Assess the morphology of the red blood cells.
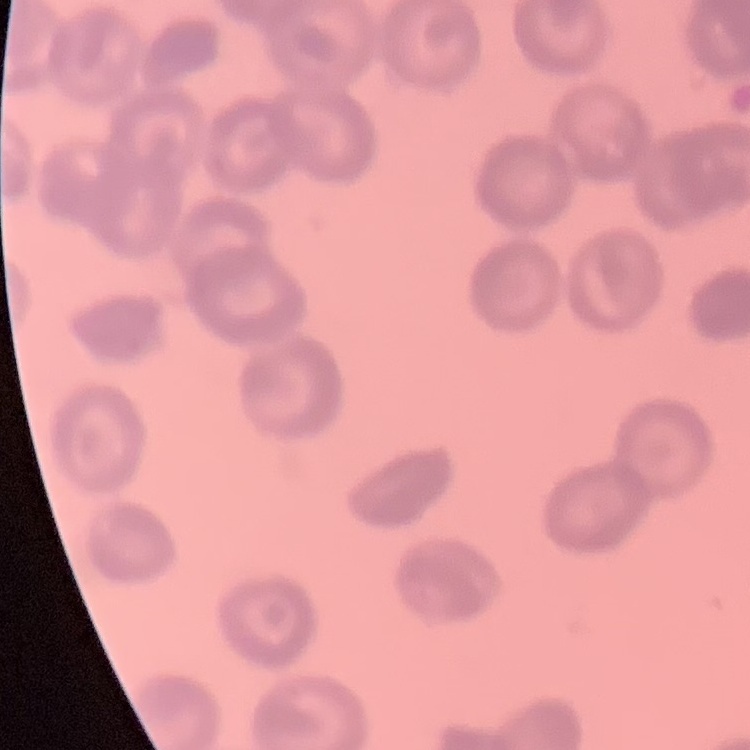

Rouleaux formation.

Summary:
  - Image type: square crop of a larger photomicrograph
  - Stain: Field's or Giemsa
  - Preparation: thin blood film